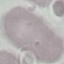
Summary:
  - Malaria status: uninfected
  - Preparation: thin smear
  - Image type: cell patch, automatically extracted from a larger field of view and resized to 64 × 64 pixels
  - Capture: smartphone camera at the microscope eyepiece
  - Stain: Giemsa